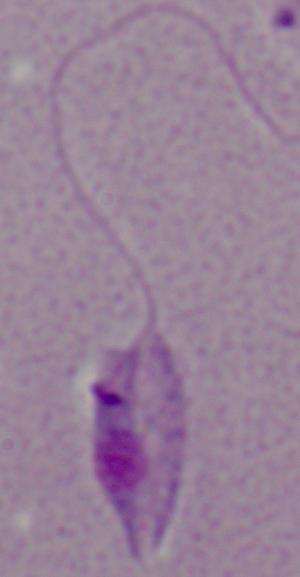

magnification = 1000x
identification = Leishmania
modality = photomicrograph